State which parasite is depicted.
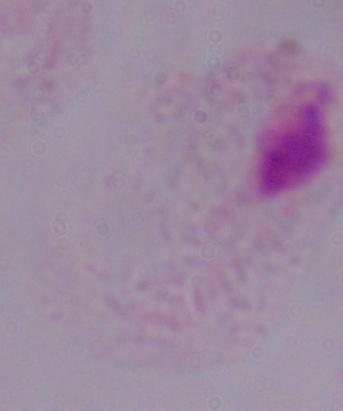
This is a trichomonad.

Micrograph. Captured at 1000x magnification.